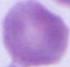
Summary:
  - Identification: red blood cell
  - Modality: photomicrograph
  - Magnification: 1000x